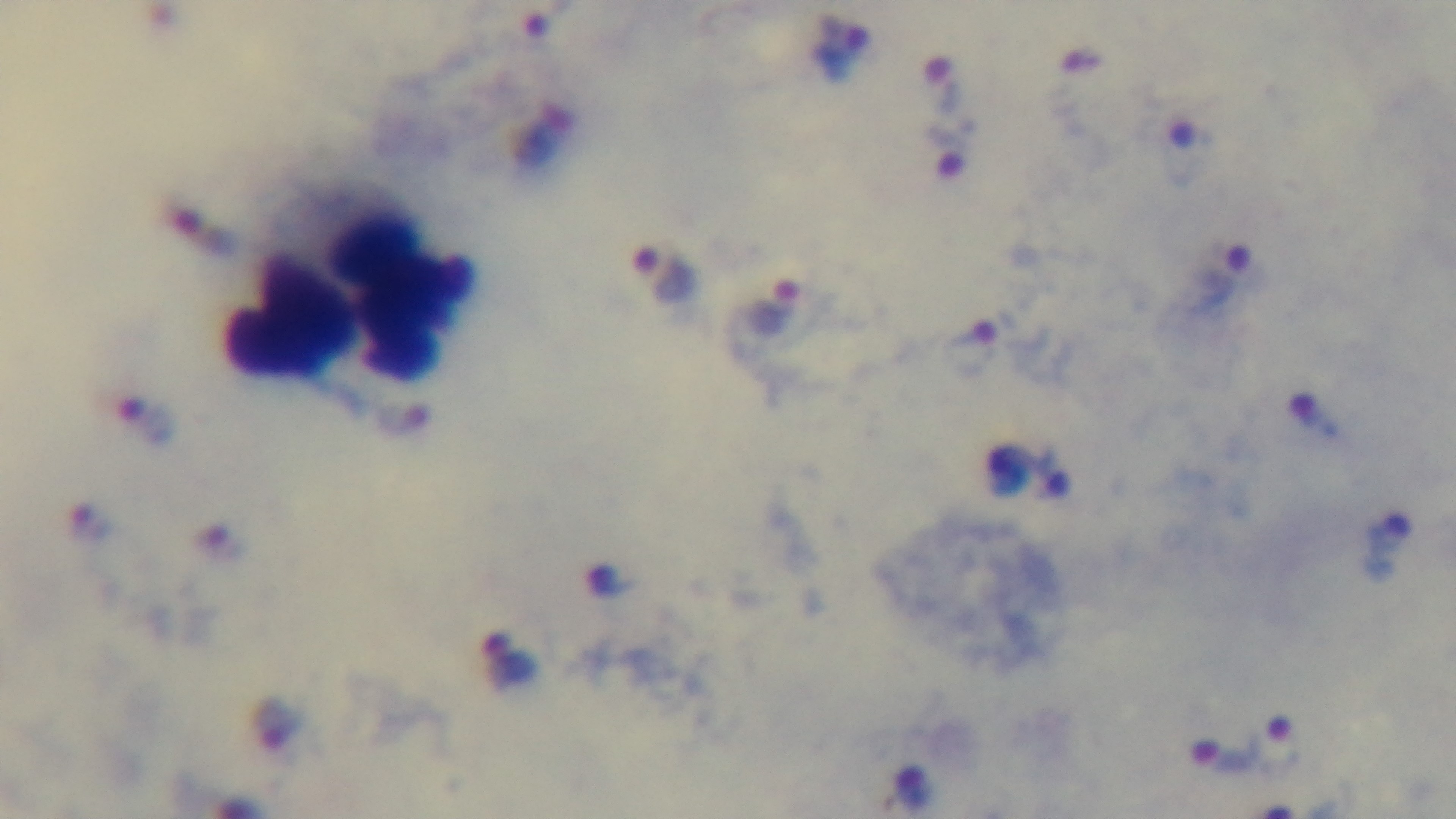
Preparation: thick. Malaria status: infected. Photomicrograph. Captured with a mounted 4K digital camera. Oil-immersion objective, 100x. Giemsa stain. Single field of view.